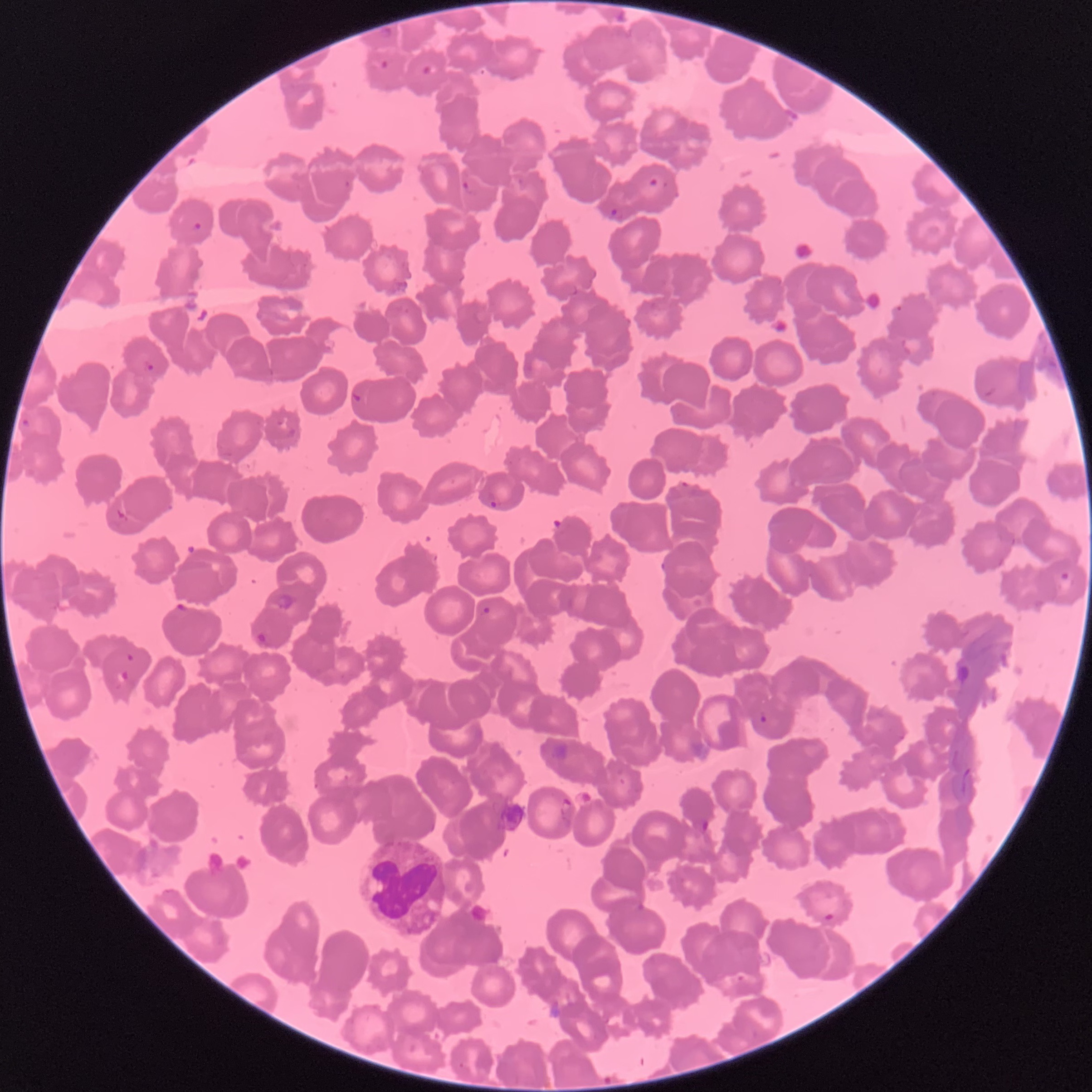

coordinate format = approximate bounding boxes as [x1, y1, x2, y2] in pixels
white blood cell locations = [356, 839, 447, 937]
Plasmodium parasite locations = [380, 28, 393, 40], [377, 57, 393, 70], [422, 64, 438, 76], [648, 177, 658, 187], [461, 179, 477, 198], [343, 180, 351, 189], [609, 208, 623, 221], [190, 220, 204, 233], [562, 283, 579, 297], [894, 303, 904, 312], [142, 359, 157, 374], [982, 387, 997, 399], [350, 391, 364, 404], [21, 417, 33, 429], [285, 427, 297, 440], [679, 479, 691, 489], [487, 492, 501, 508], [116, 508, 129, 524], [658, 561, 669, 572], [1058, 571, 1072, 584], [174, 601, 189, 614], [481, 605, 492, 616], [255, 631, 269, 648], [126, 653, 135, 662], [113, 670, 129, 684], [757, 710, 769, 724], [560, 798, 573, 827], [693, 818, 710, 835], [604, 896, 649, 917], [823, 911, 836, 924]
red blood cell morphology = rouleaux formation
image size = 1092×1092 pixels
preparation = thin blood film
modality = optical microscopy